Name the cell type shown.
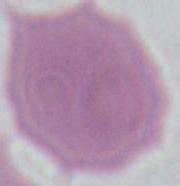
This is an erythrocyte.

modality: photomicrograph
magnification: 1000x